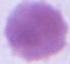

Summary:
  - Modality: photomicrograph
  - Magnification: 1000x
  - Identification: erythrocyte